Locate every blood parasite and identify its species.
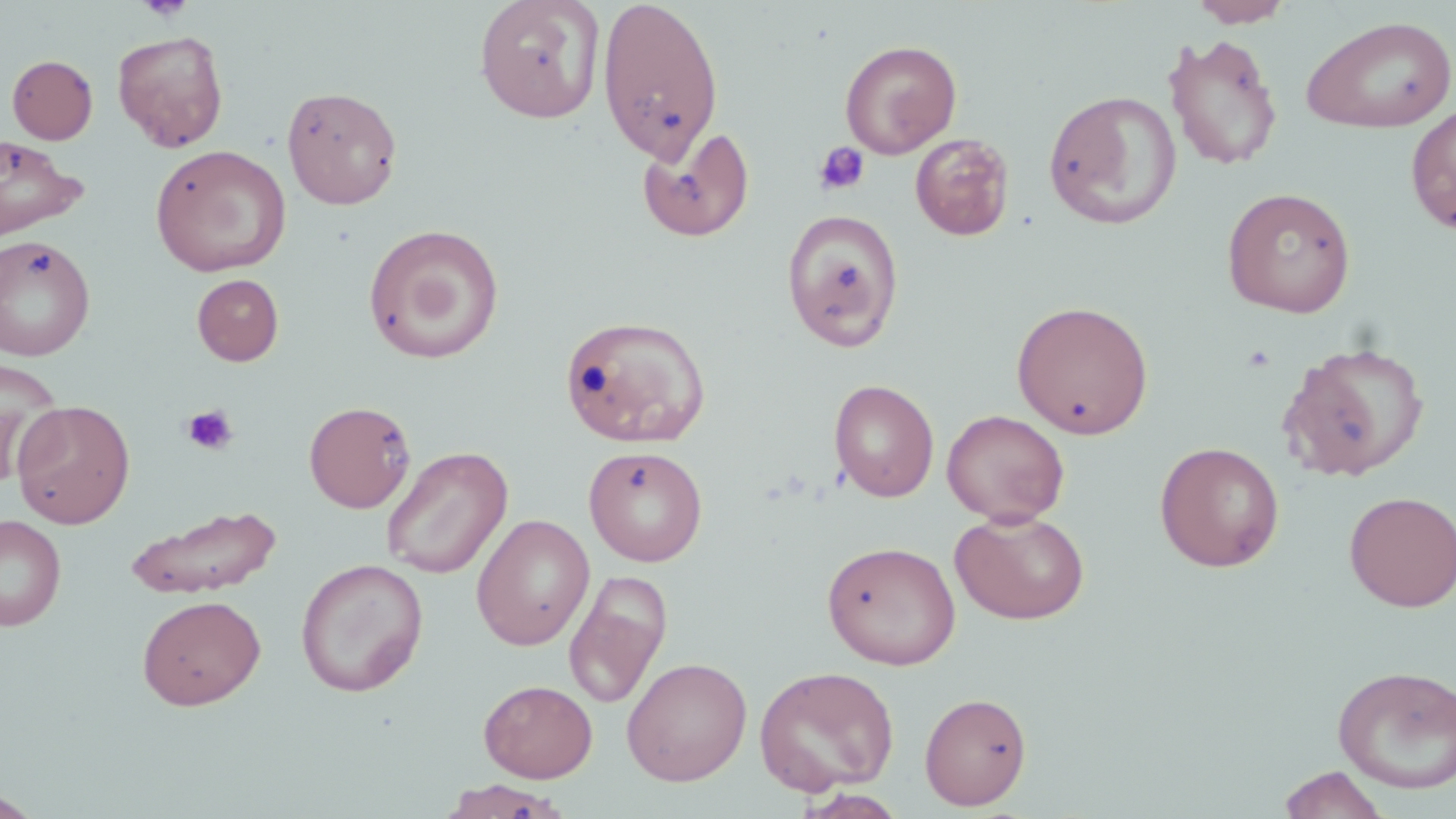

No blood parasites seen.

Summary:
  - Coordinate format: approximate bounding boxes as [x1, y1, x2, y2] in pixels
  - Uninfected red blood cell locations: [475, 0, 605, 124], [596, 0, 724, 165], [1188, 0, 1294, 27], [1300, 14, 1456, 135], [112, 29, 230, 152], [1163, 33, 1284, 171], [839, 39, 963, 159], [7, 54, 98, 144], [281, 85, 403, 210], [1043, 89, 1182, 230], [1405, 104, 1456, 234], [636, 123, 755, 242], [0, 133, 88, 240], [909, 133, 1015, 240], [150, 144, 292, 277], [1221, 186, 1357, 318], [781, 208, 906, 352], [363, 223, 505, 364], [0, 235, 95, 361], [192, 274, 284, 365], [1011, 300, 1154, 439], [560, 314, 711, 448], [1277, 341, 1431, 482], [0, 359, 66, 483], [828, 379, 940, 502], [11, 400, 135, 528], [303, 401, 416, 513], [941, 409, 1070, 526], [1154, 441, 1285, 572], [583, 445, 708, 566], [380, 446, 513, 579], [1343, 490, 1456, 612], [124, 504, 283, 599], [950, 509, 1090, 625], [0, 514, 66, 631], [471, 514, 595, 651], [822, 540, 961, 670], [295, 558, 429, 696], [564, 569, 673, 711], [137, 594, 266, 710], [621, 656, 752, 785], [1332, 665, 1456, 794], [754, 666, 900, 797], [479, 679, 598, 782], [919, 692, 1033, 810], [1277, 765, 1391, 819], [439, 779, 570, 819], [796, 789, 907, 818], [0, 790, 43, 818]
  - Platelet locations: [138, 0, 193, 22], [813, 141, 871, 197], [181, 404, 238, 455]
  - Slide-level diagnosis: no evidence of blood parasites
  - Preparation: thin blood smear
  - Modality: optical microscopy
  - Image size: 1456×819 pixels
  - Stain: May-Grünwald-Giemsa
  - Magnification: 1000x
  - Field of view: one of a larger specimen